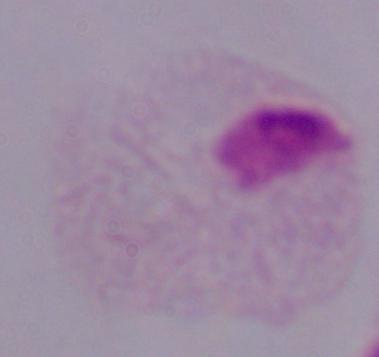

magnification: 1000x
identification: trichomonad
modality: micrograph